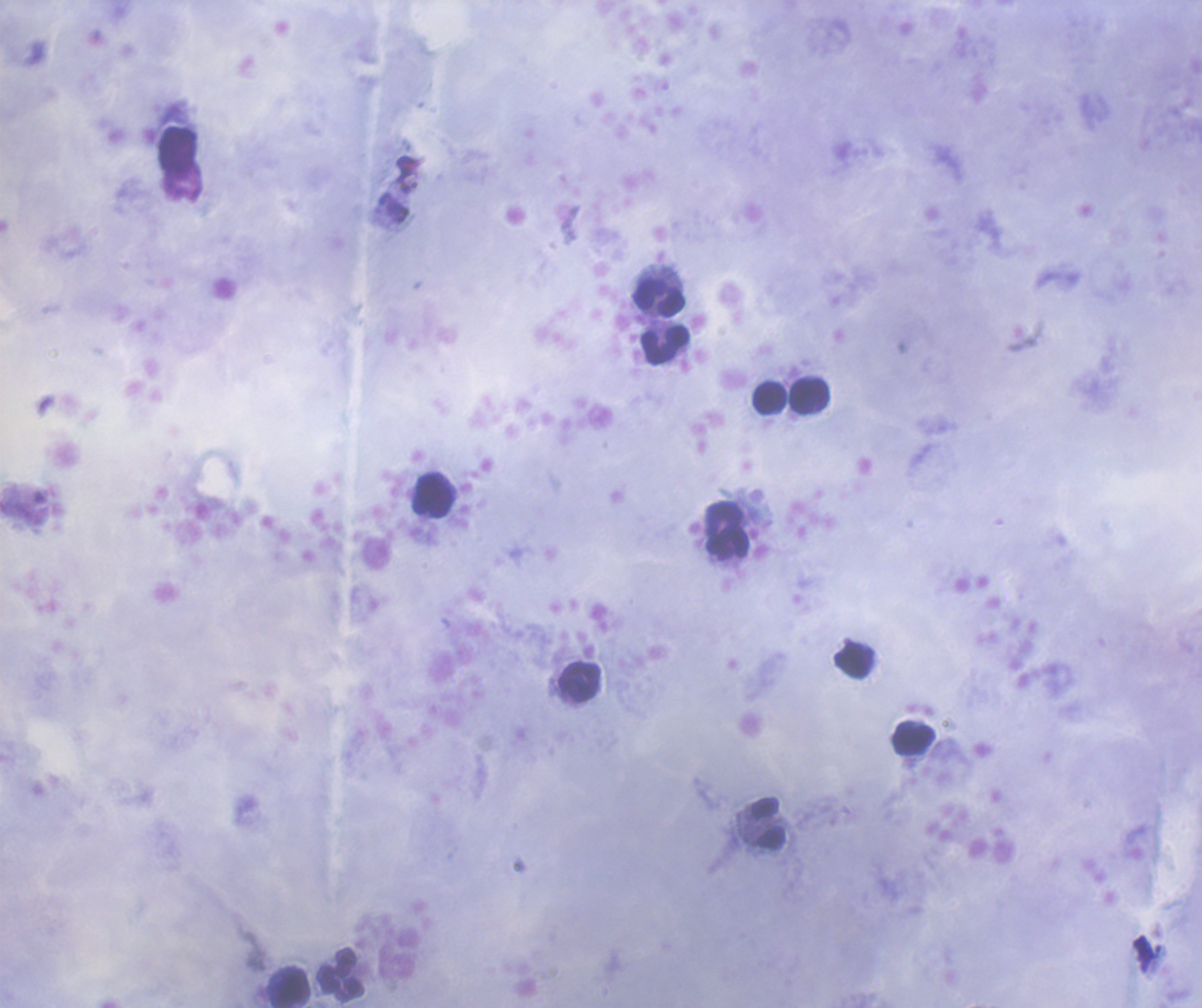
Approximate centers as [x, y] in pixels.
Summary:
  - Leukocyte locations: [657, 297], [664, 346], [810, 395], [769, 397], [434, 495], [724, 516], [727, 544], [855, 660], [581, 681], [914, 738], [767, 822], [341, 974], [290, 987]
  - Preparation: thick blood film
  - Stain: Romanowsky
  - Result: no Plasmodium parasites seen
  - Context: previously used in an actual diagnosis
  - Background quality: good
  - Field of view: single
  - Magnification: 100x
  - Coloration quality: good
  - Image size: 1202×1008 pixels